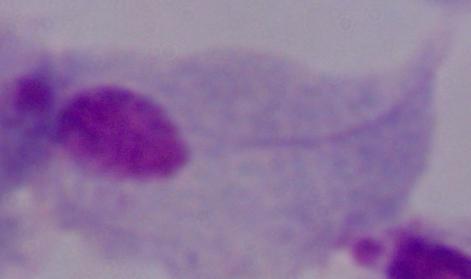

Captured at 1000x magnification. A trichomonad is shown. Micrograph.